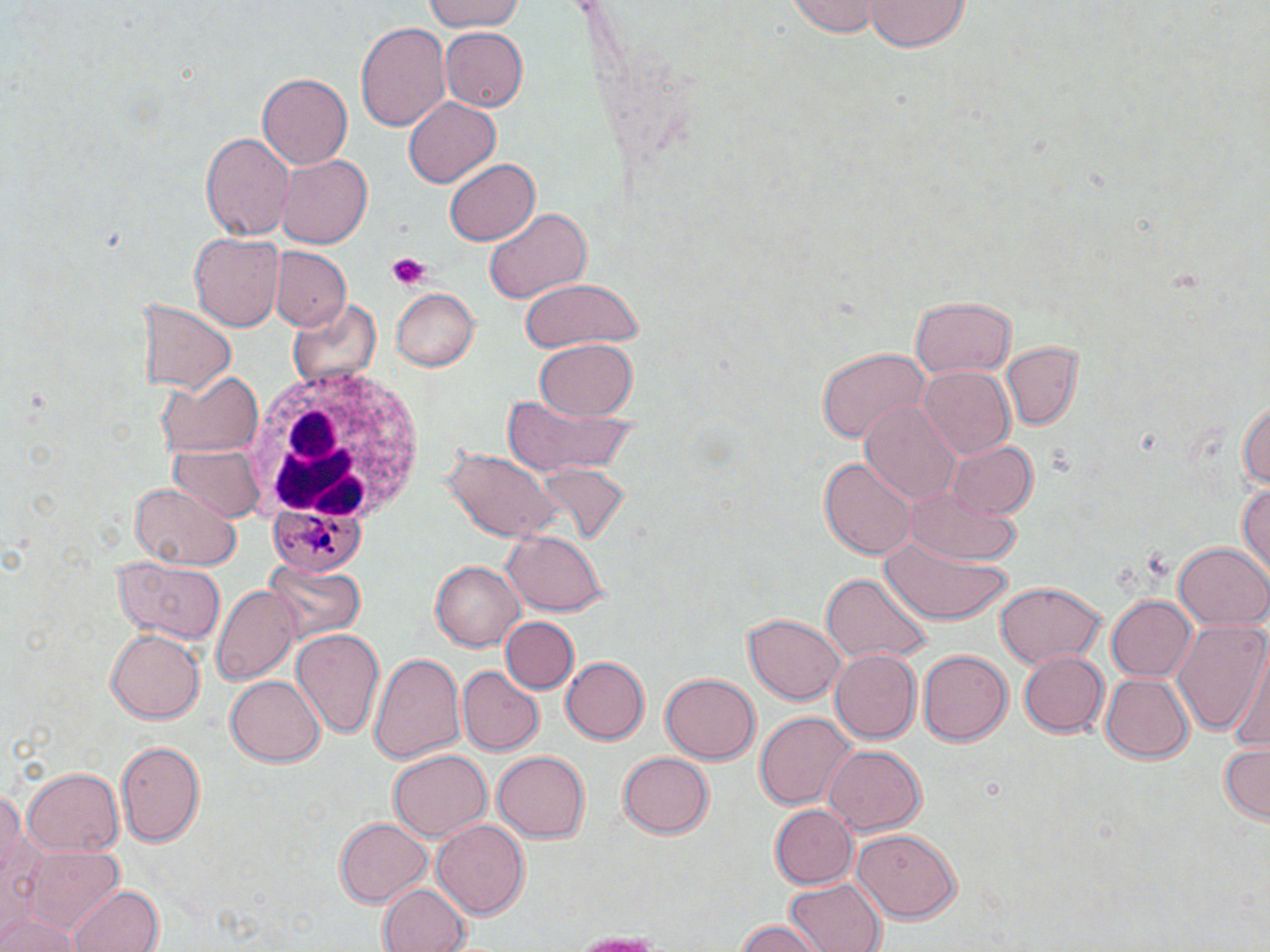

Approximate bounding boxes as named x1/y1/x2/y2 corners in pixels. Uninfected red blood cell locations: (x1=421, y1=0, x2=528, y2=33), (x1=864, y1=0, x2=967, y2=53), (x1=786, y1=1, x2=883, y2=37), (x1=356, y1=19, x2=452, y2=135), (x1=439, y1=27, x2=528, y2=112), (x1=258, y1=72, x2=351, y2=170), (x1=404, y1=95, x2=500, y2=185), (x1=201, y1=131, x2=294, y2=243), (x1=275, y1=153, x2=372, y2=250), (x1=444, y1=159, x2=541, y2=246), (x1=455, y1=169, x2=576, y2=285), (x1=484, y1=207, x2=592, y2=305), (x1=189, y1=232, x2=282, y2=332), (x1=273, y1=247, x2=350, y2=331), (x1=520, y1=275, x2=644, y2=353), (x1=390, y1=287, x2=478, y2=372), (x1=910, y1=296, x2=1016, y2=378), (x1=136, y1=298, x2=237, y2=395), (x1=288, y1=298, x2=381, y2=391), (x1=535, y1=338, x2=638, y2=421), (x1=1000, y1=340, x2=1081, y2=430), (x1=815, y1=346, x2=931, y2=445), (x1=916, y1=366, x2=1017, y2=460), (x1=157, y1=373, x2=264, y2=459), (x1=1238, y1=389, x2=1270, y2=502), (x1=504, y1=394, x2=636, y2=480), (x1=859, y1=399, x2=963, y2=507), (x1=945, y1=440, x2=1039, y2=521), (x1=443, y1=445, x2=559, y2=540), (x1=169, y1=446, x2=263, y2=521), (x1=819, y1=454, x2=915, y2=558), (x1=534, y1=463, x2=630, y2=548), (x1=1236, y1=479, x2=1270, y2=583), (x1=128, y1=483, x2=240, y2=570), (x1=903, y1=486, x2=1026, y2=567), (x1=878, y1=531, x2=1010, y2=627), (x1=501, y1=532, x2=610, y2=616), (x1=1173, y1=542, x2=1268, y2=631), (x1=262, y1=558, x2=365, y2=649), (x1=112, y1=559, x2=226, y2=644), (x1=429, y1=559, x2=525, y2=655), (x1=821, y1=574, x2=932, y2=667), (x1=993, y1=581, x2=1106, y2=669), (x1=210, y1=585, x2=301, y2=683), (x1=1108, y1=595, x2=1195, y2=681), (x1=744, y1=612, x2=847, y2=705), (x1=501, y1=616, x2=577, y2=693), (x1=1173, y1=617, x2=1269, y2=737), (x1=105, y1=629, x2=204, y2=723), (x1=293, y1=629, x2=385, y2=738), (x1=1226, y1=648, x2=1270, y2=756), (x1=829, y1=649, x2=923, y2=745), (x1=369, y1=650, x2=466, y2=769), (x1=919, y1=650, x2=1013, y2=747), (x1=1017, y1=650, x2=1108, y2=739), (x1=560, y1=656, x2=652, y2=746), (x1=457, y1=665, x2=544, y2=756), (x1=228, y1=673, x2=324, y2=765), (x1=1100, y1=675, x2=1194, y2=764), (x1=657, y1=676, x2=759, y2=766), (x1=754, y1=710, x2=855, y2=810), (x1=116, y1=738, x2=206, y2=849), (x1=1216, y1=742, x2=1269, y2=823), (x1=822, y1=744, x2=924, y2=834), (x1=389, y1=750, x2=492, y2=842), (x1=492, y1=750, x2=592, y2=845), (x1=615, y1=750, x2=716, y2=841), (x1=21, y1=766, x2=124, y2=856), (x1=0, y1=786, x2=35, y2=927), (x1=770, y1=804, x2=858, y2=888), (x1=334, y1=816, x2=431, y2=909), (x1=433, y1=818, x2=531, y2=921), (x1=853, y1=827, x2=962, y2=923), (x1=23, y1=845, x2=125, y2=933), (x1=783, y1=877, x2=883, y2=952), (x1=377, y1=881, x2=469, y2=952), (x1=67, y1=884, x2=164, y2=952), (x1=0, y1=908, x2=80, y2=952), (x1=731, y1=918, x2=825, y2=952), (x1=564, y1=930, x2=670, y2=951). White blood cell locations: (x1=247, y1=363, x2=431, y2=530). Plasmodium malariae-infected red blood cell locations: (x1=266, y1=502, x2=372, y2=574). Platelet locations: (x1=384, y1=253, x2=434, y2=291). Slide-level diagnosis: Plasmodium malariae. Light microscopy. May-Grünwald-Giemsa-stained preparation. Captured at 1000x magnification. Image is 1270×952 pixels. Thin blood film. One field of a larger specimen.